Locate and identify every blood parasite.
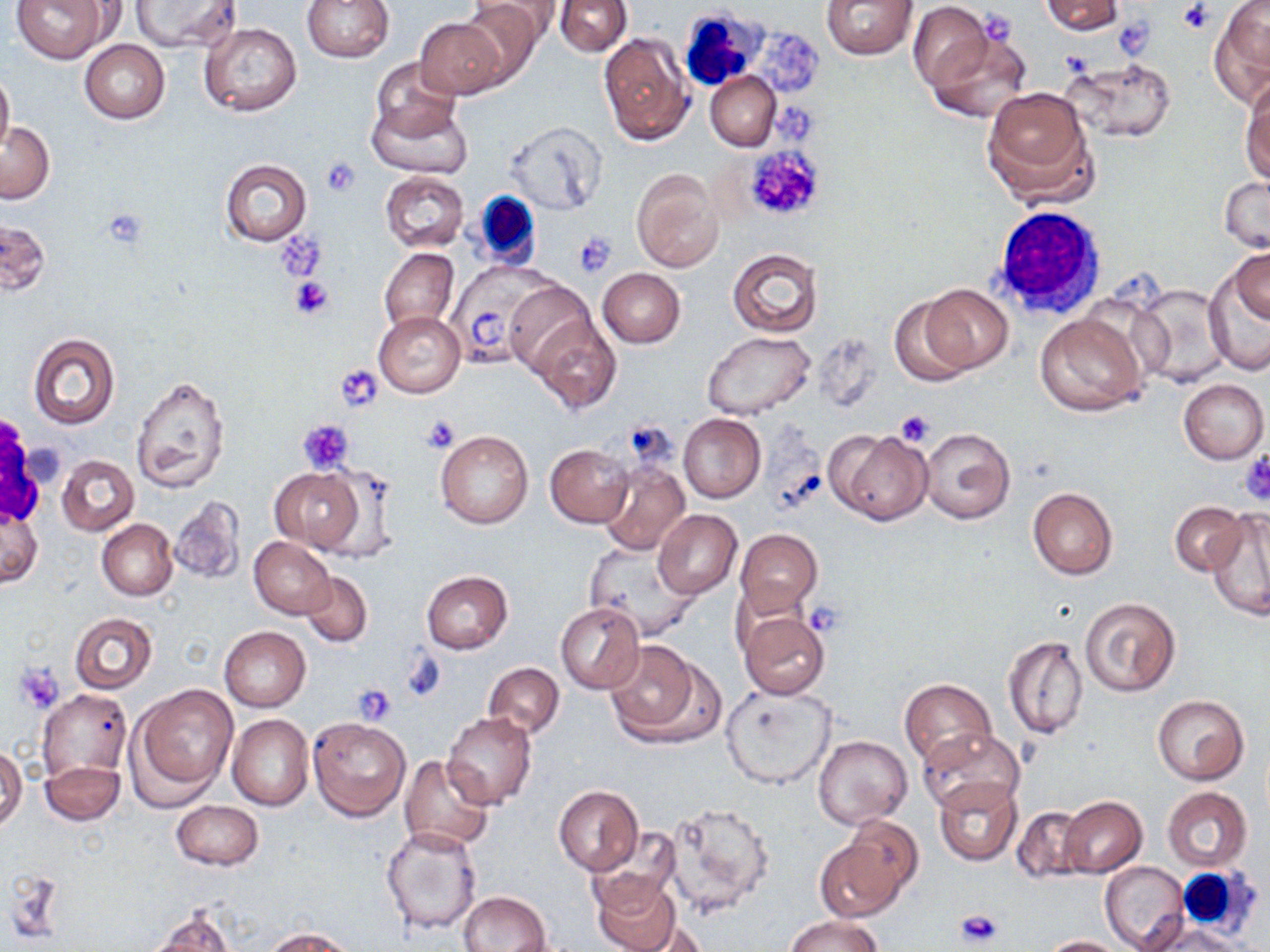
No blood parasites seen.

Approximate bounding boxes as [x1, y1, x2, y2] in pixels. White blood cell locations: [676, 9, 767, 92], [463, 191, 551, 267], [989, 205, 1109, 322], [1176, 867, 1257, 933]. Uninfected red blood cell locations: [13, 0, 109, 63], [131, 0, 241, 52], [303, 0, 394, 62], [475, 0, 563, 50], [821, 0, 918, 60], [1038, 0, 1125, 35], [456, 1, 545, 86], [555, 1, 631, 57], [1209, 1, 1270, 105], [907, 3, 992, 91], [413, 17, 509, 99], [199, 22, 301, 117], [923, 27, 1034, 125], [597, 30, 692, 146], [80, 40, 169, 123], [1061, 55, 1176, 143], [370, 56, 461, 143], [0, 66, 14, 156], [705, 71, 781, 151], [1241, 78, 1270, 188], [980, 85, 1096, 206], [368, 97, 471, 180], [503, 120, 608, 215], [0, 121, 53, 204], [220, 158, 311, 246], [631, 168, 724, 271], [379, 171, 468, 251], [1220, 176, 1269, 255], [0, 219, 51, 295], [378, 246, 458, 336], [1230, 247, 1270, 330], [727, 248, 823, 337], [1209, 251, 1270, 369], [445, 262, 548, 369], [596, 268, 685, 347], [502, 278, 600, 381], [1128, 283, 1236, 388], [921, 284, 1012, 372], [889, 298, 973, 387], [373, 311, 465, 398], [1035, 311, 1147, 417], [530, 313, 621, 413], [702, 331, 814, 421], [27, 333, 120, 430], [130, 375, 231, 493], [1179, 379, 1267, 463], [678, 413, 765, 503], [919, 428, 1015, 523], [827, 429, 933, 524], [436, 430, 533, 530], [545, 443, 635, 528], [57, 455, 139, 535], [598, 463, 688, 556], [317, 464, 401, 565], [270, 467, 364, 551], [1027, 487, 1119, 579], [170, 497, 246, 584], [1170, 502, 1248, 577], [1, 505, 42, 589], [99, 509, 240, 589], [653, 509, 741, 599], [1208, 509, 1270, 620], [98, 519, 177, 600], [735, 528, 822, 614], [248, 536, 335, 618], [583, 541, 702, 641], [299, 570, 371, 646], [420, 570, 513, 654], [1078, 597, 1181, 697], [556, 601, 645, 693], [739, 610, 831, 700], [69, 613, 157, 693], [220, 625, 310, 712], [1002, 633, 1090, 741], [604, 640, 706, 743], [483, 662, 565, 739], [899, 678, 997, 769], [134, 682, 239, 792], [722, 684, 836, 790], [37, 690, 133, 781], [1152, 694, 1249, 784], [442, 712, 536, 809], [227, 714, 313, 810], [307, 716, 410, 821], [918, 728, 1025, 816], [814, 737, 911, 828], [0, 745, 26, 829], [398, 755, 495, 852], [41, 760, 125, 824], [933, 777, 1022, 866], [553, 784, 644, 876], [1162, 787, 1253, 872], [1059, 796, 1147, 878], [171, 800, 264, 871], [660, 800, 774, 917], [1012, 806, 1088, 883], [841, 816, 923, 901], [380, 825, 484, 934], [588, 831, 680, 910], [816, 836, 908, 922], [1099, 862, 1189, 951], [589, 874, 684, 952], [458, 891, 551, 952], [146, 908, 236, 951], [783, 914, 885, 952], [1140, 917, 1245, 951], [262, 927, 356, 952], [1040, 935, 1127, 952]. Platelet locations: [1177, 0, 1213, 34], [1114, 17, 1156, 56], [740, 144, 826, 222], [320, 159, 359, 196], [101, 204, 150, 251], [573, 231, 615, 276], [278, 232, 325, 282], [289, 275, 336, 320], [336, 368, 383, 413], [895, 410, 936, 447], [420, 414, 461, 452], [625, 418, 678, 467], [298, 419, 354, 475], [1240, 451, 1270, 504], [803, 601, 846, 635], [399, 649, 446, 703], [16, 664, 65, 712], [354, 685, 397, 725], [956, 907, 1003, 948]. Slide-level diagnosis: negative for blood parasites. May-Grünwald-Giemsa stain. Thin blood film. One field of a larger specimen. Optical microscopy. Captured at 1000x magnification. Image is 1270×952 pixels.